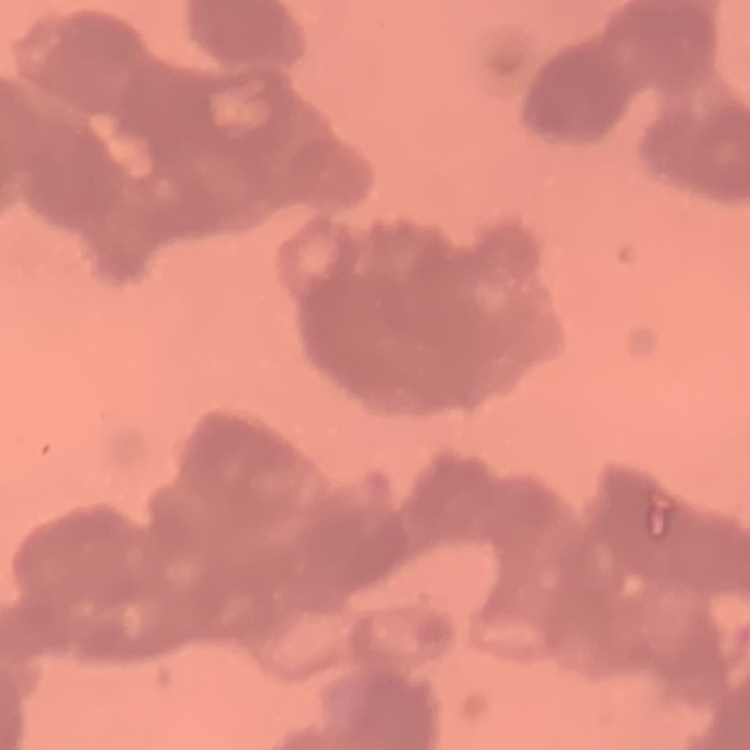
{
  "red_blood_cell_morphology": "rouleaux formation",
  "image_type": "one tile cut from a larger photomicrograph",
  "preparation": "thin blood smear",
  "stain": "Field's or Giemsa"
}